State the blood parasite species.
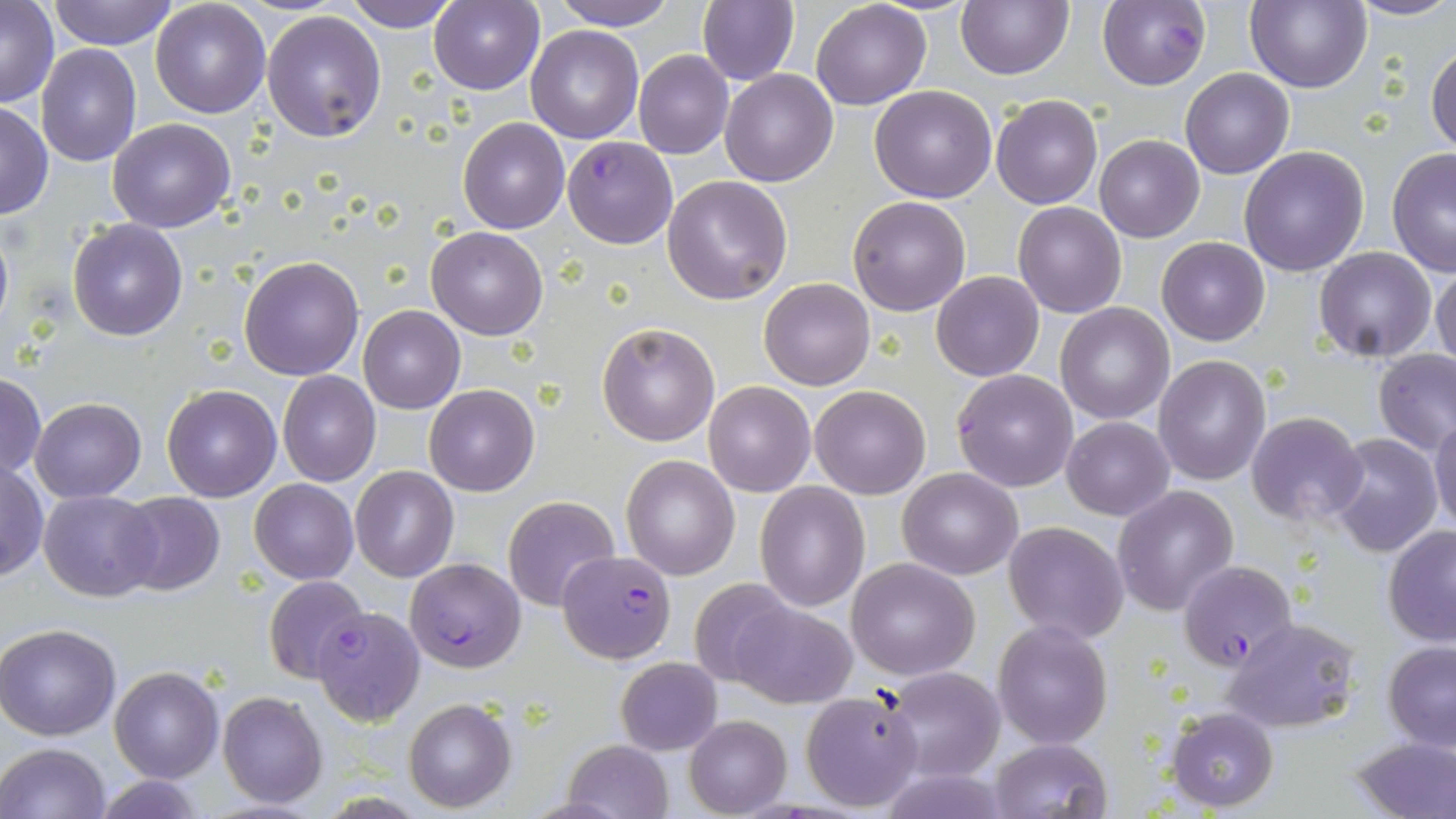

Plasmodium falciparum.

{
  "preparation": "thin blood film",
  "image_size": "1456×819 pixels",
  "stain": "May-Grünwald-Giemsa",
  "uninfected_red_blood_cell_locations": "approximate bounding boxes as named x1/y1/x2/y2 corners in pixels: (x1=50, y1=0, x2=178, y2=50), (x1=150, y1=0, x2=271, y2=118), (x1=548, y1=0, x2=679, y2=30), (x1=955, y1=0, x2=1073, y2=80), (x1=1245, y1=0, x2=1371, y2=93), (x1=1344, y1=0, x2=1456, y2=22), (x1=1, y1=1, x2=58, y2=107), (x1=346, y1=1, x2=459, y2=32), (x1=428, y1=1, x2=544, y2=95), (x1=697, y1=1, x2=798, y2=86), (x1=810, y1=1, x2=931, y2=110), (x1=261, y1=9, x2=387, y2=143), (x1=527, y1=25, x2=643, y2=144), (x1=1426, y1=41, x2=1456, y2=156), (x1=36, y1=43, x2=141, y2=166), (x1=633, y1=50, x2=733, y2=159), (x1=1180, y1=67, x2=1293, y2=179), (x1=720, y1=68, x2=838, y2=186), (x1=869, y1=84, x2=998, y2=202), (x1=991, y1=94, x2=1103, y2=209), (x1=0, y1=102, x2=52, y2=221), (x1=107, y1=118, x2=237, y2=233), (x1=457, y1=118, x2=569, y2=234), (x1=1095, y1=135, x2=1205, y2=243), (x1=1239, y1=147, x2=1370, y2=277), (x1=1386, y1=151, x2=1456, y2=277), (x1=663, y1=175, x2=793, y2=305), (x1=847, y1=196, x2=971, y2=316), (x1=1012, y1=203, x2=1126, y2=318), (x1=68, y1=218, x2=187, y2=341), (x1=0, y1=220, x2=14, y2=343), (x1=425, y1=225, x2=549, y2=340), (x1=1157, y1=236, x2=1270, y2=345), (x1=1315, y1=247, x2=1437, y2=363), (x1=239, y1=255, x2=364, y2=380), (x1=1431, y1=262, x2=1456, y2=373), (x1=932, y1=271, x2=1043, y2=382), (x1=759, y1=278, x2=875, y2=390), (x1=1056, y1=303, x2=1175, y2=423), (x1=358, y1=306, x2=465, y2=413), (x1=597, y1=321, x2=720, y2=447), (x1=1373, y1=348, x2=1456, y2=456), (x1=1153, y1=356, x2=1271, y2=485), (x1=277, y1=370, x2=381, y2=486), (x1=0, y1=373, x2=46, y2=480), (x1=703, y1=380, x2=814, y2=496), (x1=424, y1=383, x2=539, y2=496), (x1=162, y1=384, x2=282, y2=502), (x1=808, y1=385, x2=930, y2=499), (x1=31, y1=397, x2=146, y2=502), (x1=1246, y1=411, x2=1367, y2=527), (x1=1429, y1=415, x2=1456, y2=534), (x1=1063, y1=416, x2=1176, y2=521), (x1=1326, y1=433, x2=1442, y2=557), (x1=621, y1=455, x2=740, y2=581), (x1=1, y1=460, x2=48, y2=582), (x1=350, y1=465, x2=458, y2=582), (x1=898, y1=467, x2=1021, y2=579), (x1=250, y1=478, x2=357, y2=584), (x1=755, y1=481, x2=868, y2=612), (x1=1111, y1=484, x2=1239, y2=616), (x1=39, y1=489, x2=159, y2=601), (x1=115, y1=491, x2=225, y2=595), (x1=503, y1=495, x2=620, y2=611), (x1=1003, y1=521, x2=1129, y2=644), (x1=1383, y1=525, x2=1456, y2=648), (x1=846, y1=557, x2=981, y2=679), (x1=263, y1=576, x2=371, y2=684), (x1=688, y1=579, x2=798, y2=689), (x1=727, y1=602, x2=855, y2=707), (x1=1223, y1=617, x2=1360, y2=734), (x1=993, y1=621, x2=1113, y2=749), (x1=0, y1=623, x2=121, y2=741), (x1=1382, y1=641, x2=1456, y2=751), (x1=616, y1=657, x2=720, y2=755), (x1=881, y1=665, x2=1006, y2=782), (x1=110, y1=666, x2=224, y2=782), (x1=799, y1=689, x2=924, y2=813), (x1=218, y1=691, x2=329, y2=809), (x1=403, y1=697, x2=517, y2=813), (x1=1165, y1=707, x2=1279, y2=812), (x1=684, y1=714, x2=791, y2=817), (x1=1348, y1=735, x2=1456, y2=818), (x1=987, y1=738, x2=1112, y2=818), (x1=562, y1=740, x2=674, y2=819), (x1=0, y1=743, x2=112, y2=819), (x1=87, y1=775, x2=213, y2=818)",
  "modality": "optical microscopy",
  "field_of_view": "one of a larger specimen",
  "magnification": "1000x",
  "plasmodium_falciparum_infected_red_blood_cell_locations": "approximate bounding boxes as named x1/y1/x2/y2 corners in pixels: (x1=1097, y1=1, x2=1210, y2=90), (x1=562, y1=137, x2=677, y2=249), (x1=952, y1=368, x2=1079, y2=493), (x1=559, y1=549, x2=675, y2=664), (x1=403, y1=558, x2=525, y2=673), (x1=1178, y1=560, x2=1296, y2=671), (x1=313, y1=606, x2=425, y2=726)"
}